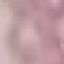
Summary:
  - Result: negative for malaria parasites
  - Preparation: thin smear
  - Image type: cell patch, automatically extracted from a larger field of view and resized to 64 × 64 pixels
  - Capture: smartphone through the microscope eyepiece
  - Stain: Giemsa